Assess this cell for malaria.
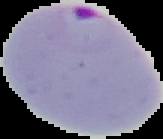
It is parasitized.

image size = 163×139 pixels
image type = segmented cell region with the area outside set to black
preparation = thin blood smear